Identify the cell.
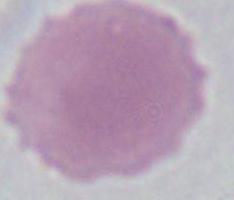
An erythrocyte.

Captured at 1000x magnification. Micrograph.